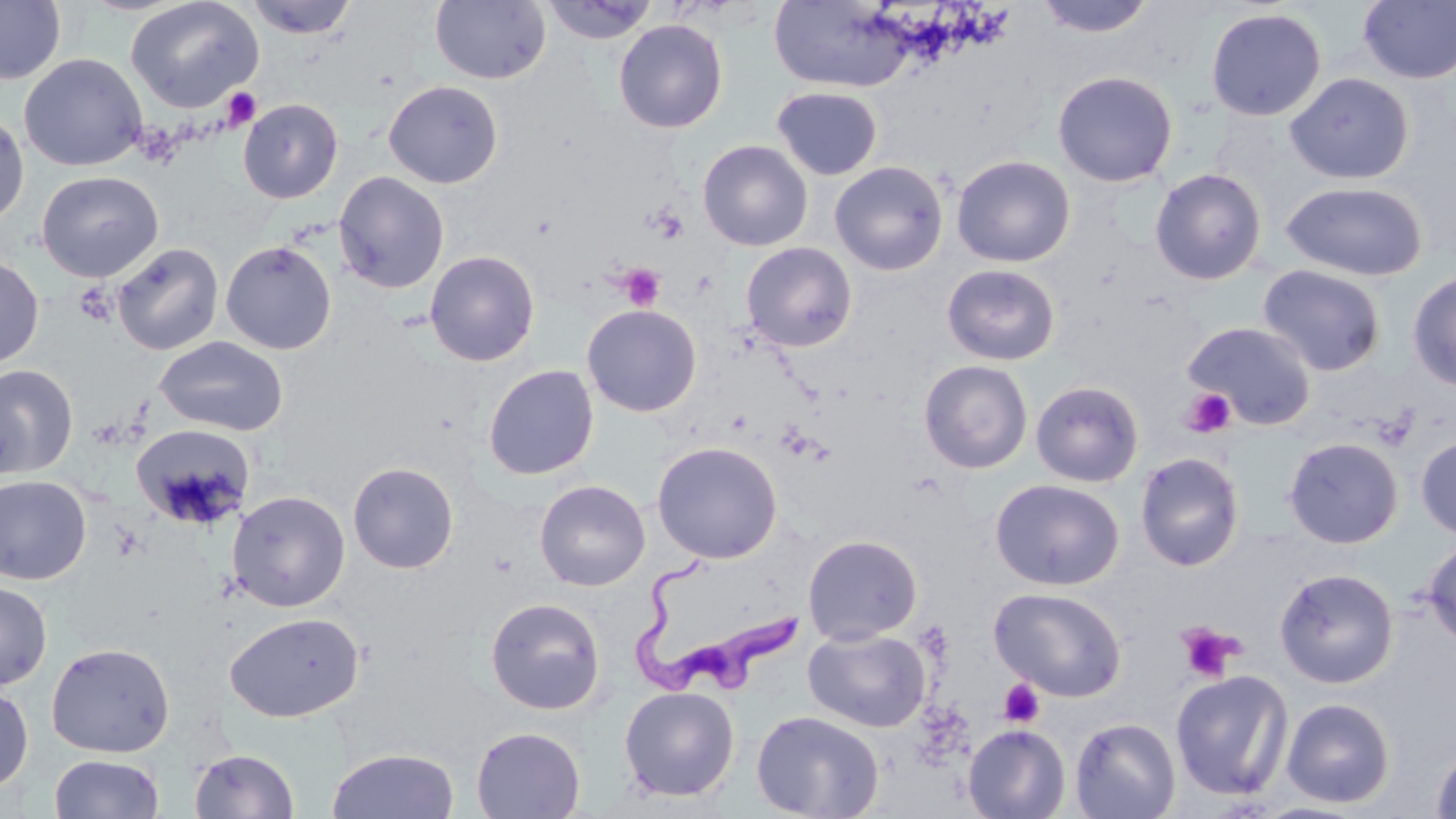 Approximate bounding boxes as (x1,y1)-(x2,y2) corner pairs in pixels. Uninfected red blood cell locations: (0,0)-(66,85), (126,0)-(264,113), (244,0)-(359,38), (430,0)-(550,85), (542,0)-(659,45), (769,0)-(917,93), (1035,0)-(1156,38), (1358,1)-(1456,85), (1205,7)-(1327,122), (613,19)-(727,134), (19,53)-(147,171), (1053,71)-(1177,188), (1285,72)-(1414,185), (383,80)-(503,189), (773,87)-(882,180), (237,98)-(343,203), (0,109)-(29,227), (698,140)-(813,251), (951,155)-(1075,267), (829,161)-(948,276), (1150,168)-(1266,285), (37,170)-(163,282), (333,170)-(449,293), (1281,182)-(1428,281), (220,240)-(337,354), (112,242)-(224,355), (741,242)-(858,351), (425,250)-(540,367), (0,255)-(44,369), (941,264)-(1060,366), (1257,264)-(1386,377), (1407,269)-(1456,392), (581,304)-(702,417), (1183,321)-(1317,431), (153,335)-(289,436), (918,359)-(1033,473), (0,363)-(78,478), (482,364)-(599,480), (1031,380)-(1144,487), (131,423)-(255,529), (1416,435)-(1456,541), (1284,437)-(1403,548), (651,441)-(783,563), (1135,452)-(1244,572), (348,461)-(459,574), (0,475)-(92,585), (990,479)-(1124,590), (535,480)-(650,591), (227,490)-(350,612), (802,534)-(923,645), (1422,536)-(1456,650), (1274,568)-(1398,688), (0,581)-(52,690), (989,587)-(1127,702), (485,597)-(606,715), (225,612)-(365,723), (803,628)-(930,732), (46,641)-(175,758), (1170,670)-(1293,802), (0,682)-(34,794), (618,685)-(740,802), (1281,698)-(1395,808), (751,710)-(884,819), (1069,717)-(1181,818), (963,724)-(1071,818), (470,725)-(586,819), (1429,741)-(1456,819), (326,747)-(460,819), (189,748)-(300,818), (49,754)-(163,818). Platelet locations: (222,87)-(262,130), (648,206)-(688,243), (620,264)-(665,311), (1180,388)-(1236,439), (1176,621)-(1244,684), (998,679)-(1045,728). Trypanosoma brucei locations: (630,556)-(803,702). Slide-level diagnosis: Trypanosoma brucei. Image is 1456×819 pixels. One field of a larger specimen. Optical microscopy. Thin blood smear. 1000x magnification. May-Grünwald-Giemsa-stained preparation.